Report the malaria status of this cell.
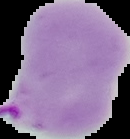
Parasitized.

Image is 130×139 pixels. From a thin blood film. Segmented cell region on a black background.